Locate every Plasmodium falciparum-infected red blood cell.
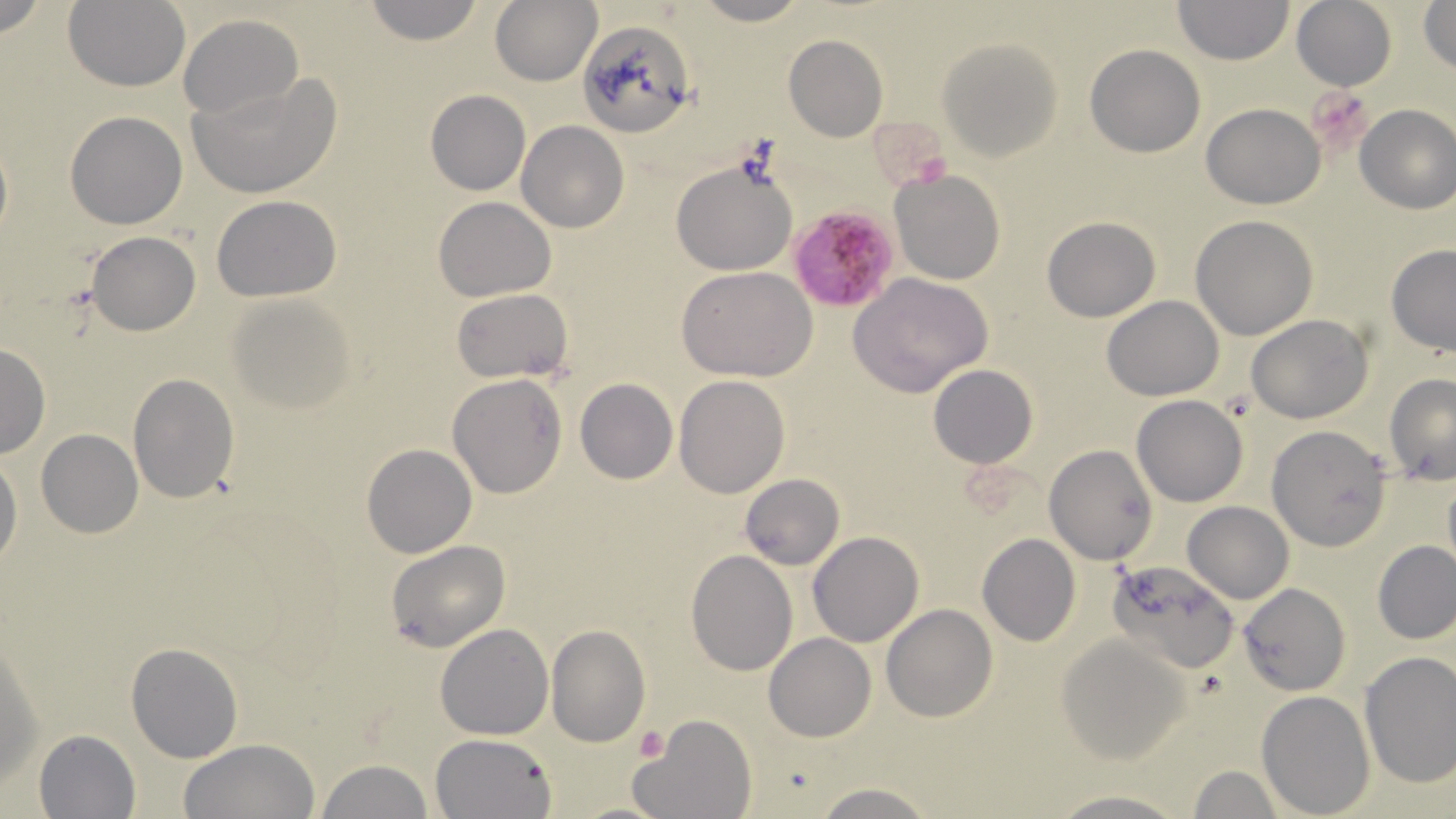
Approximate bounding boxes as (x1, y1, x2, y2) in pixels.
Plasmodium falciparum-infected red blood cells: (789, 205, 900, 310).

Summary:
  - Platelet locations: (1309, 89, 1376, 153), (634, 725, 669, 762)
  - Uninfected red blood cell locations: (362, 0, 485, 45), (490, 0, 602, 87), (689, 0, 809, 26), (1173, 0, 1294, 66), (1418, 0, 1456, 73), (62, 1, 190, 91), (1290, 1, 1397, 91), (178, 14, 303, 118), (580, 20, 695, 137), (783, 34, 887, 142), (939, 37, 1062, 162), (1086, 44, 1206, 158), (191, 74, 338, 197), (426, 90, 531, 194), (1353, 102, 1456, 214), (1201, 104, 1326, 209), (66, 110, 187, 230), (517, 122, 629, 233), (671, 158, 797, 275), (890, 168, 1006, 286), (212, 196, 341, 301), (433, 196, 556, 302), (1190, 215, 1318, 339), (1043, 216, 1161, 321), (87, 232, 200, 335), (1385, 244, 1456, 355), (679, 267, 817, 381), (848, 273, 994, 397), (451, 288, 573, 382), (227, 293, 359, 412), (1101, 296, 1225, 401), (1245, 313, 1372, 424), (0, 343, 50, 459), (929, 364, 1038, 469), (128, 372, 240, 505), (447, 373, 568, 499), (674, 374, 790, 497), (1384, 374, 1456, 485), (575, 379, 676, 484), (1132, 395, 1248, 507), (1268, 425, 1394, 550), (37, 429, 143, 538), (361, 444, 477, 559), (1044, 444, 1157, 565), (0, 453, 23, 569), (741, 474, 844, 569), (1182, 501, 1294, 603), (808, 530, 924, 647), (977, 532, 1080, 647), (1372, 540, 1456, 645), (386, 541, 511, 652), (685, 551, 797, 675), (1108, 557, 1238, 674), (1238, 583, 1351, 695), (881, 603, 998, 722), (436, 623, 553, 740), (545, 625, 650, 746), (1, 630, 44, 798), (763, 633, 877, 741), (1057, 634, 1192, 765), (126, 642, 243, 762), (1358, 651, 1456, 788), (1258, 689, 1374, 816), (636, 715, 755, 819), (33, 729, 141, 817), (430, 732, 557, 818), (178, 738, 322, 819), (315, 759, 437, 819), (1189, 765, 1284, 818), (811, 781, 940, 818), (1045, 790, 1192, 818)
  - Slide-level diagnosis: Plasmodium falciparum
  - Image size: 1456×819 pixels
  - Magnification: 1000x
  - Modality: light microscopy
  - Stain: May-Grünwald-Giemsa
  - Preparation: thin blood smear
  - Field of view: one of a larger specimen